State the blood parasite species.
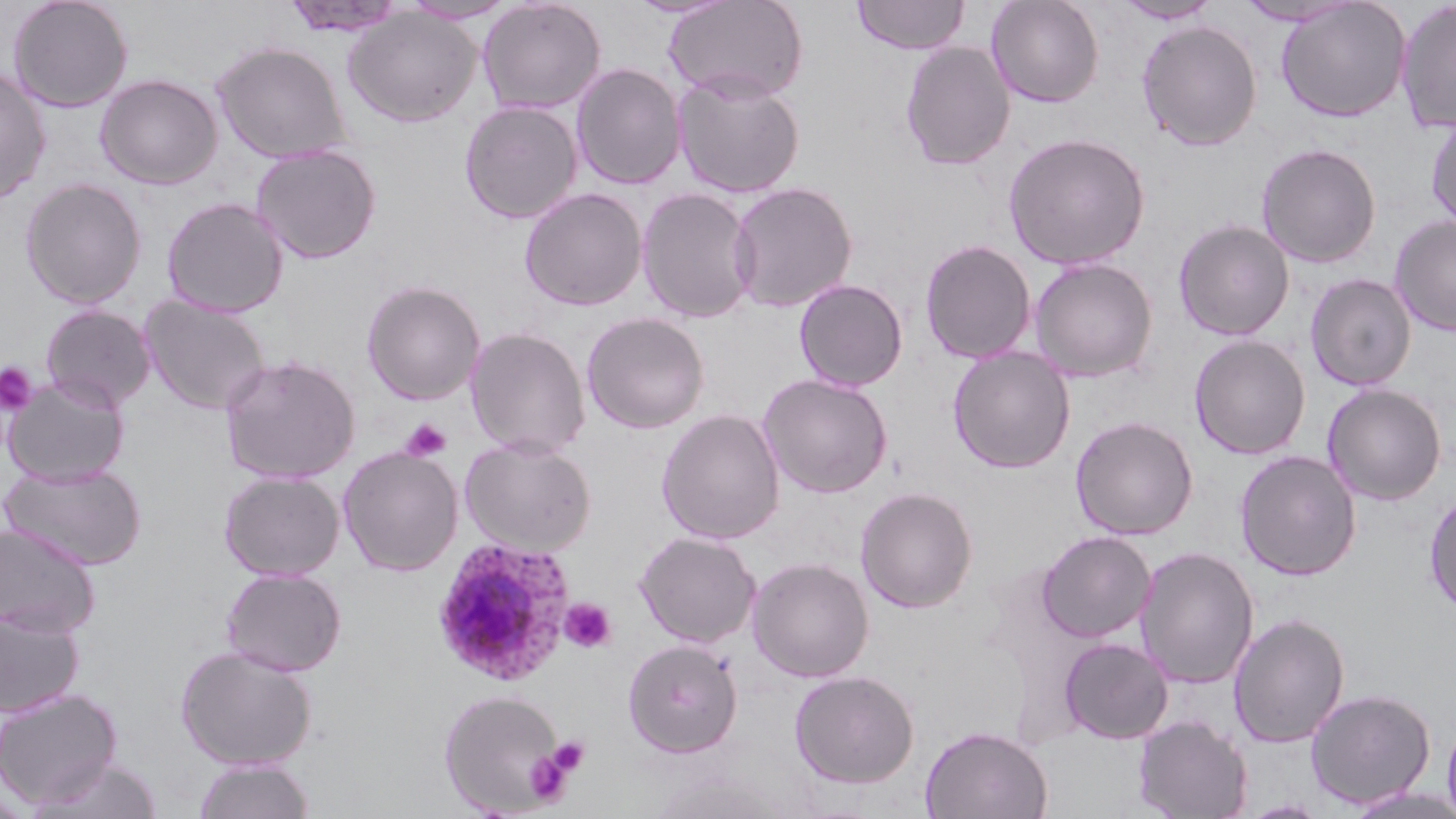

Plasmodium ovale.

Summary:
  - Coordinate format: approximate bounding boxes as named x1/y1/x2/y2 corners in pixels
  - Plasmodium ovale-infected red blood cell locations: (x1=430, y1=536, x2=577, y2=686)
  - Uninfected red blood cell locations: (x1=7, y1=0, x2=134, y2=113), (x1=278, y1=0, x2=409, y2=38), (x1=477, y1=0, x2=607, y2=115), (x1=663, y1=0, x2=809, y2=103), (x1=851, y1=0, x2=970, y2=55), (x1=985, y1=0, x2=1104, y2=108), (x1=1113, y1=0, x2=1221, y2=24), (x1=1234, y1=0, x2=1358, y2=26), (x1=1275, y1=0, x2=1411, y2=122), (x1=401, y1=1, x2=518, y2=24), (x1=1395, y1=1, x2=1456, y2=133), (x1=343, y1=7, x2=481, y2=128), (x1=1137, y1=20, x2=1263, y2=151), (x1=900, y1=40, x2=1016, y2=171), (x1=211, y1=41, x2=352, y2=163), (x1=571, y1=63, x2=687, y2=190), (x1=0, y1=65, x2=52, y2=206), (x1=95, y1=73, x2=223, y2=190), (x1=673, y1=73, x2=805, y2=199), (x1=459, y1=100, x2=584, y2=224), (x1=1425, y1=113, x2=1456, y2=231), (x1=1003, y1=132, x2=1152, y2=270), (x1=1256, y1=143, x2=1382, y2=268), (x1=251, y1=144, x2=382, y2=264), (x1=20, y1=178, x2=147, y2=309), (x1=728, y1=181, x2=858, y2=313), (x1=637, y1=186, x2=759, y2=324), (x1=519, y1=187, x2=648, y2=311), (x1=162, y1=197, x2=289, y2=318), (x1=1389, y1=214, x2=1456, y2=337), (x1=1173, y1=219, x2=1295, y2=341), (x1=919, y1=239, x2=1037, y2=363), (x1=1029, y1=257, x2=1158, y2=382), (x1=1305, y1=273, x2=1417, y2=391), (x1=794, y1=278, x2=908, y2=392), (x1=361, y1=280, x2=485, y2=405), (x1=139, y1=295, x2=271, y2=415), (x1=40, y1=304, x2=156, y2=411), (x1=581, y1=311, x2=709, y2=434), (x1=464, y1=326, x2=592, y2=459), (x1=1189, y1=334, x2=1311, y2=459), (x1=948, y1=346, x2=1076, y2=473), (x1=220, y1=354, x2=360, y2=484), (x1=757, y1=373, x2=893, y2=498), (x1=2, y1=374, x2=129, y2=487), (x1=1322, y1=383, x2=1447, y2=506), (x1=657, y1=409, x2=785, y2=544), (x1=1070, y1=416, x2=1198, y2=541), (x1=460, y1=437, x2=597, y2=555), (x1=338, y1=445, x2=463, y2=576), (x1=1234, y1=450, x2=1361, y2=582), (x1=1, y1=461, x2=147, y2=570), (x1=219, y1=470, x2=345, y2=581), (x1=855, y1=486, x2=978, y2=613), (x1=1424, y1=490, x2=1456, y2=619), (x1=0, y1=523, x2=100, y2=637), (x1=1036, y1=530, x2=1156, y2=643), (x1=634, y1=531, x2=761, y2=648), (x1=1135, y1=546, x2=1259, y2=689), (x1=748, y1=557, x2=874, y2=682), (x1=220, y1=567, x2=347, y2=677), (x1=0, y1=606, x2=85, y2=718), (x1=1228, y1=613, x2=1350, y2=748), (x1=1058, y1=637, x2=1173, y2=744), (x1=623, y1=638, x2=743, y2=758), (x1=175, y1=644, x2=319, y2=770), (x1=789, y1=670, x2=919, y2=789), (x1=0, y1=688, x2=122, y2=809), (x1=1305, y1=688, x2=1436, y2=809), (x1=438, y1=689, x2=569, y2=815), (x1=1442, y1=714, x2=1456, y2=819), (x1=1133, y1=715, x2=1252, y2=819), (x1=920, y1=725, x2=1052, y2=819), (x1=30, y1=755, x2=165, y2=818), (x1=192, y1=757, x2=315, y2=819)
  - Platelet locations: (x1=0, y1=363, x2=38, y2=414), (x1=400, y1=418, x2=452, y2=461), (x1=558, y1=597, x2=617, y2=653), (x1=547, y1=737, x2=590, y2=776), (x1=523, y1=746, x2=573, y2=805)
  - Field of view: one of a larger specimen
  - Modality: optical microscopy
  - Magnification: 1000x
  - Image size: 1456×819 pixels
  - Stain: May-Grünwald-Giemsa
  - Preparation: thin blood smear